Give the extent of all Plasmodium vivax-infected red blood cells.
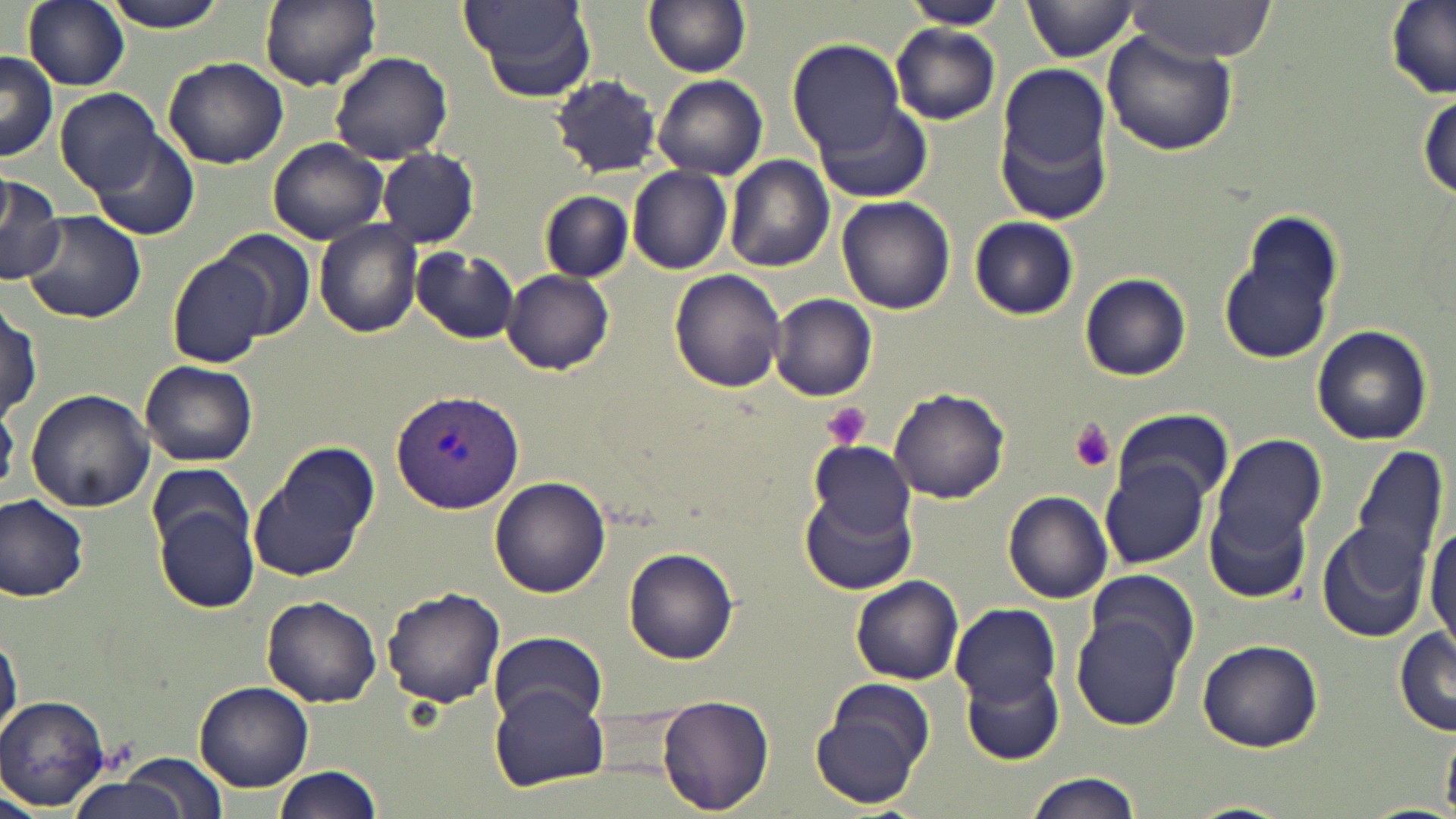
Approximate bounding boxes as named x1/y1/x2/y2 corners in pixels.
Plasmodium vivax-infected red blood cells: (x1=390, y1=389, x2=525, y2=514).

Platelet locations: (x1=821, y1=402, x2=872, y2=450), (x1=1069, y1=421, x2=1118, y2=472). Uninfected red blood cell locations: (x1=21, y1=0, x2=129, y2=90), (x1=98, y1=0, x2=233, y2=32), (x1=258, y1=0, x2=380, y2=90), (x1=459, y1=0, x2=595, y2=101), (x1=644, y1=0, x2=752, y2=78), (x1=905, y1=0, x2=1007, y2=29), (x1=1022, y1=0, x2=1141, y2=62), (x1=1127, y1=1, x2=1281, y2=62), (x1=1385, y1=4, x2=1455, y2=103), (x1=890, y1=23, x2=1002, y2=124), (x1=1101, y1=29, x2=1238, y2=157), (x1=788, y1=39, x2=907, y2=157), (x1=0, y1=51, x2=59, y2=163), (x1=329, y1=51, x2=452, y2=164), (x1=162, y1=56, x2=288, y2=169), (x1=997, y1=64, x2=1113, y2=209), (x1=654, y1=74, x2=768, y2=179), (x1=549, y1=75, x2=663, y2=177), (x1=54, y1=89, x2=166, y2=197), (x1=1418, y1=91, x2=1455, y2=202), (x1=815, y1=100, x2=934, y2=202), (x1=86, y1=133, x2=201, y2=241), (x1=267, y1=138, x2=389, y2=247), (x1=376, y1=147, x2=480, y2=248), (x1=724, y1=156, x2=835, y2=272), (x1=626, y1=166, x2=734, y2=274), (x1=0, y1=173, x2=65, y2=286), (x1=540, y1=190, x2=634, y2=283), (x1=837, y1=196, x2=957, y2=315), (x1=19, y1=210, x2=146, y2=323), (x1=1218, y1=215, x2=1344, y2=368), (x1=968, y1=216, x2=1080, y2=320), (x1=314, y1=220, x2=424, y2=338), (x1=216, y1=228, x2=317, y2=339), (x1=411, y1=247, x2=520, y2=343), (x1=167, y1=253, x2=276, y2=366), (x1=668, y1=269, x2=788, y2=394), (x1=502, y1=270, x2=615, y2=375), (x1=1079, y1=272, x2=1192, y2=381), (x1=769, y1=294, x2=878, y2=400), (x1=1, y1=299, x2=40, y2=425), (x1=1313, y1=324, x2=1433, y2=445), (x1=140, y1=359, x2=257, y2=467), (x1=25, y1=389, x2=154, y2=513), (x1=887, y1=389, x2=1009, y2=505), (x1=1111, y1=407, x2=1233, y2=503), (x1=1213, y1=436, x2=1326, y2=546), (x1=809, y1=442, x2=917, y2=539), (x1=1350, y1=443, x2=1448, y2=577), (x1=247, y1=451, x2=374, y2=583), (x1=147, y1=462, x2=257, y2=569), (x1=1104, y1=464, x2=1212, y2=570), (x1=489, y1=476, x2=612, y2=597), (x1=799, y1=488, x2=916, y2=596), (x1=0, y1=491, x2=92, y2=601), (x1=1003, y1=492, x2=1114, y2=604), (x1=153, y1=495, x2=262, y2=615), (x1=1204, y1=503, x2=1312, y2=604), (x1=1316, y1=520, x2=1431, y2=642), (x1=1425, y1=523, x2=1455, y2=648), (x1=624, y1=545, x2=738, y2=665), (x1=1087, y1=568, x2=1199, y2=673), (x1=851, y1=575, x2=964, y2=685), (x1=382, y1=587, x2=507, y2=710), (x1=261, y1=595, x2=382, y2=708), (x1=952, y1=602, x2=1060, y2=705), (x1=1073, y1=613, x2=1185, y2=729), (x1=1, y1=626, x2=21, y2=743), (x1=1394, y1=626, x2=1456, y2=736), (x1=488, y1=630, x2=609, y2=726), (x1=1197, y1=639, x2=1323, y2=753), (x1=963, y1=665, x2=1064, y2=766), (x1=194, y1=680, x2=315, y2=790), (x1=489, y1=687, x2=610, y2=790), (x1=810, y1=693, x2=928, y2=810), (x1=656, y1=694, x2=773, y2=814), (x1=1, y1=695, x2=111, y2=810), (x1=1443, y1=726, x2=1455, y2=814), (x1=122, y1=754, x2=229, y2=819), (x1=272, y1=765, x2=383, y2=819), (x1=1023, y1=772, x2=1143, y2=819), (x1=61, y1=775, x2=195, y2=819), (x1=0, y1=792, x2=43, y2=819), (x1=1188, y1=798, x2=1294, y2=818). Slide-level diagnosis: Plasmodium vivax. Captured at 1000x magnification. Image is 1456×819 pixels. One field of a larger specimen. May-Grünwald-Giemsa stain. Thin blood smear. Optical microscopy.